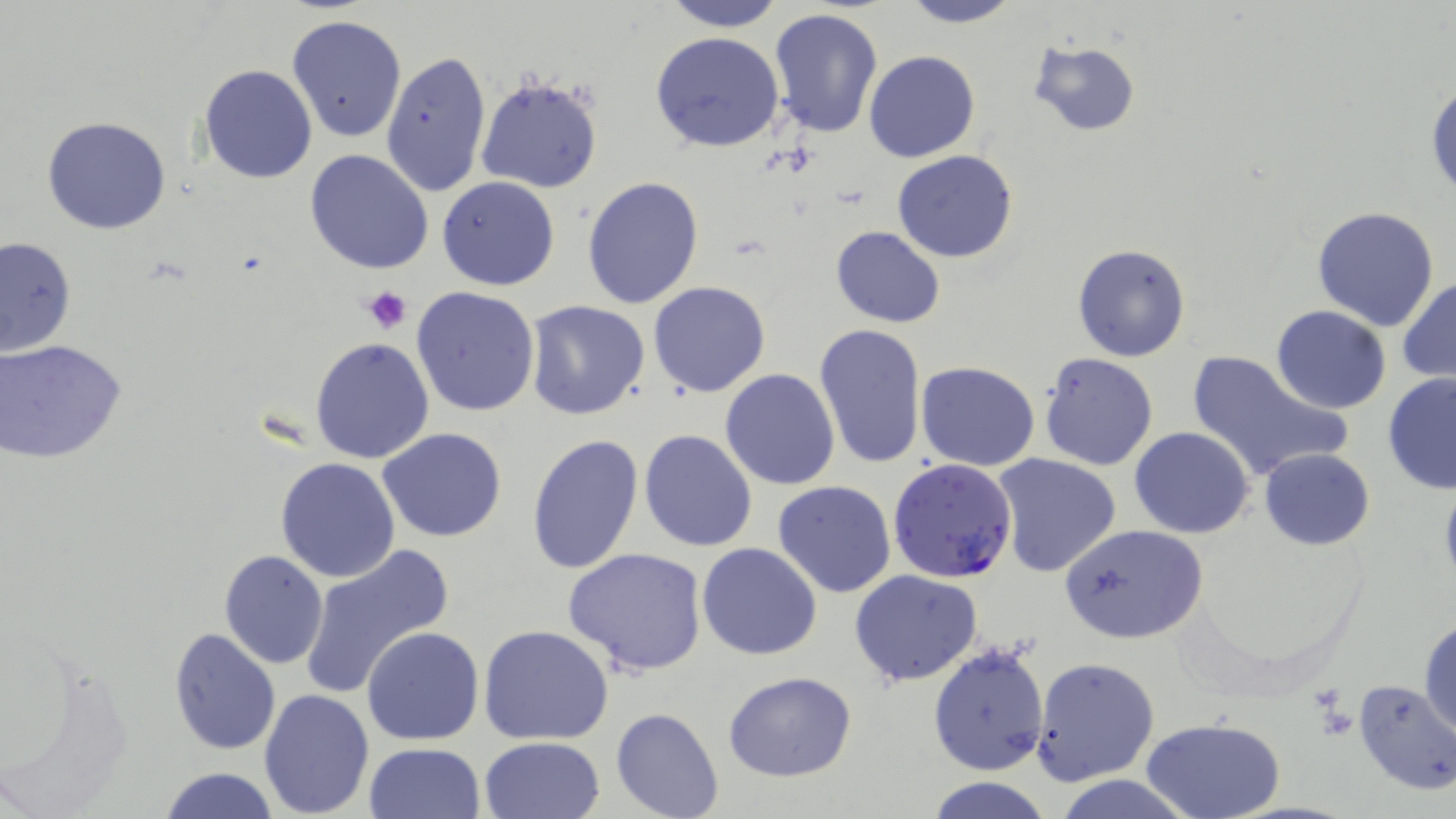 Approximate bounding boxes as named x1/y1/x2/y2 corners in pixels. Uninfected red blood cell locations: (x1=660, y1=0, x2=787, y2=31), (x1=897, y1=0, x2=1023, y2=28), (x1=767, y1=7, x2=883, y2=139), (x1=288, y1=16, x2=407, y2=142), (x1=651, y1=31, x2=784, y2=153), (x1=1027, y1=38, x2=1140, y2=135), (x1=380, y1=49, x2=491, y2=198), (x1=864, y1=50, x2=981, y2=163), (x1=198, y1=63, x2=317, y2=183), (x1=476, y1=73, x2=603, y2=195), (x1=1426, y1=81, x2=1456, y2=200), (x1=42, y1=116, x2=172, y2=235), (x1=305, y1=150, x2=434, y2=276), (x1=892, y1=150, x2=1019, y2=262), (x1=437, y1=176, x2=560, y2=290), (x1=581, y1=176, x2=704, y2=309), (x1=1311, y1=206, x2=1440, y2=331), (x1=830, y1=228, x2=945, y2=327), (x1=0, y1=236, x2=75, y2=356), (x1=1072, y1=243, x2=1191, y2=361), (x1=1398, y1=278, x2=1456, y2=384), (x1=648, y1=280, x2=770, y2=397), (x1=411, y1=285, x2=541, y2=417), (x1=525, y1=301, x2=650, y2=420), (x1=1271, y1=306, x2=1393, y2=414), (x1=813, y1=323, x2=925, y2=472), (x1=311, y1=338, x2=434, y2=464), (x1=0, y1=341, x2=127, y2=464), (x1=1186, y1=350, x2=1351, y2=484), (x1=1040, y1=353, x2=1160, y2=472), (x1=916, y1=360, x2=1040, y2=470), (x1=720, y1=368, x2=841, y2=490), (x1=1381, y1=373, x2=1456, y2=493), (x1=378, y1=427, x2=507, y2=544), (x1=1129, y1=427, x2=1254, y2=538), (x1=639, y1=429, x2=758, y2=552), (x1=527, y1=434, x2=644, y2=578), (x1=1259, y1=448, x2=1374, y2=550), (x1=992, y1=453, x2=1123, y2=578), (x1=275, y1=457, x2=402, y2=583), (x1=772, y1=481, x2=897, y2=598), (x1=1062, y1=524, x2=1208, y2=645), (x1=696, y1=543, x2=822, y2=660), (x1=299, y1=544, x2=454, y2=697), (x1=563, y1=547, x2=708, y2=676), (x1=218, y1=549, x2=329, y2=670), (x1=849, y1=569, x2=984, y2=687), (x1=1420, y1=618, x2=1455, y2=737), (x1=478, y1=624, x2=613, y2=745), (x1=362, y1=626, x2=484, y2=746), (x1=168, y1=627, x2=281, y2=755), (x1=927, y1=643, x2=1050, y2=776), (x1=1031, y1=656, x2=1160, y2=786), (x1=722, y1=671, x2=857, y2=781), (x1=1352, y1=680, x2=1456, y2=795), (x1=259, y1=688, x2=375, y2=816), (x1=610, y1=706, x2=724, y2=819), (x1=1142, y1=718, x2=1284, y2=819), (x1=477, y1=736, x2=606, y2=819), (x1=365, y1=742, x2=486, y2=819), (x1=160, y1=767, x2=279, y2=819), (x1=928, y1=777, x2=1052, y2=819). Platelet locations: (x1=363, y1=287, x2=413, y2=334). Plasmodium falciparum-infected red blood cell locations: (x1=886, y1=458, x2=1018, y2=584). Slide-level diagnosis: Plasmodium falciparum. 1000x magnification. Light microscopy. May-Grünwald-Giemsa-stained preparation. Image is 1456×819 pixels. Thin blood smear. Single field of view.